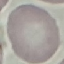 Malaria status: uninfected. Acquired by smartphone through the microscope eyepiece. Giemsa stain. Thin smear of blood. Automatically extracted cell patch, resized to 64 × 64 pixels.